State which parasite is depicted.
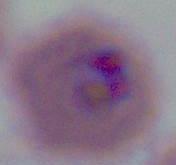
Plasmodium.

Summary:
  - Magnification: 400x or 1000x
  - Modality: micrograph